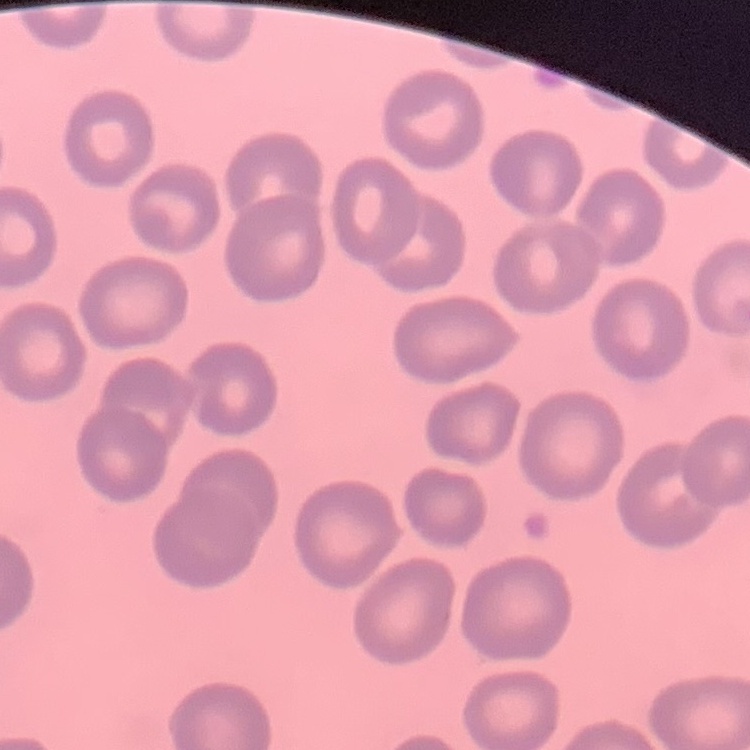
The erythrocytes exhibit no rouleaux formation. Thin blood smear. Stained with either Field's or Giemsa. One tile cut from a larger photomicrograph.